Classify this cell by malaria status.
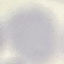

It is uninfected.

preparation = thin smear
capture = smartphone camera at the microscope eyepiece
stain = Giemsa
image type = cell patch, automatically extracted from a larger field of view and resized to 64 × 64 pixels